State which parasite is depicted.
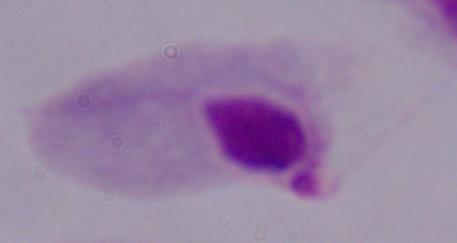
This is a trichomonad.

Captured at 1000x magnification. Photomicrograph.